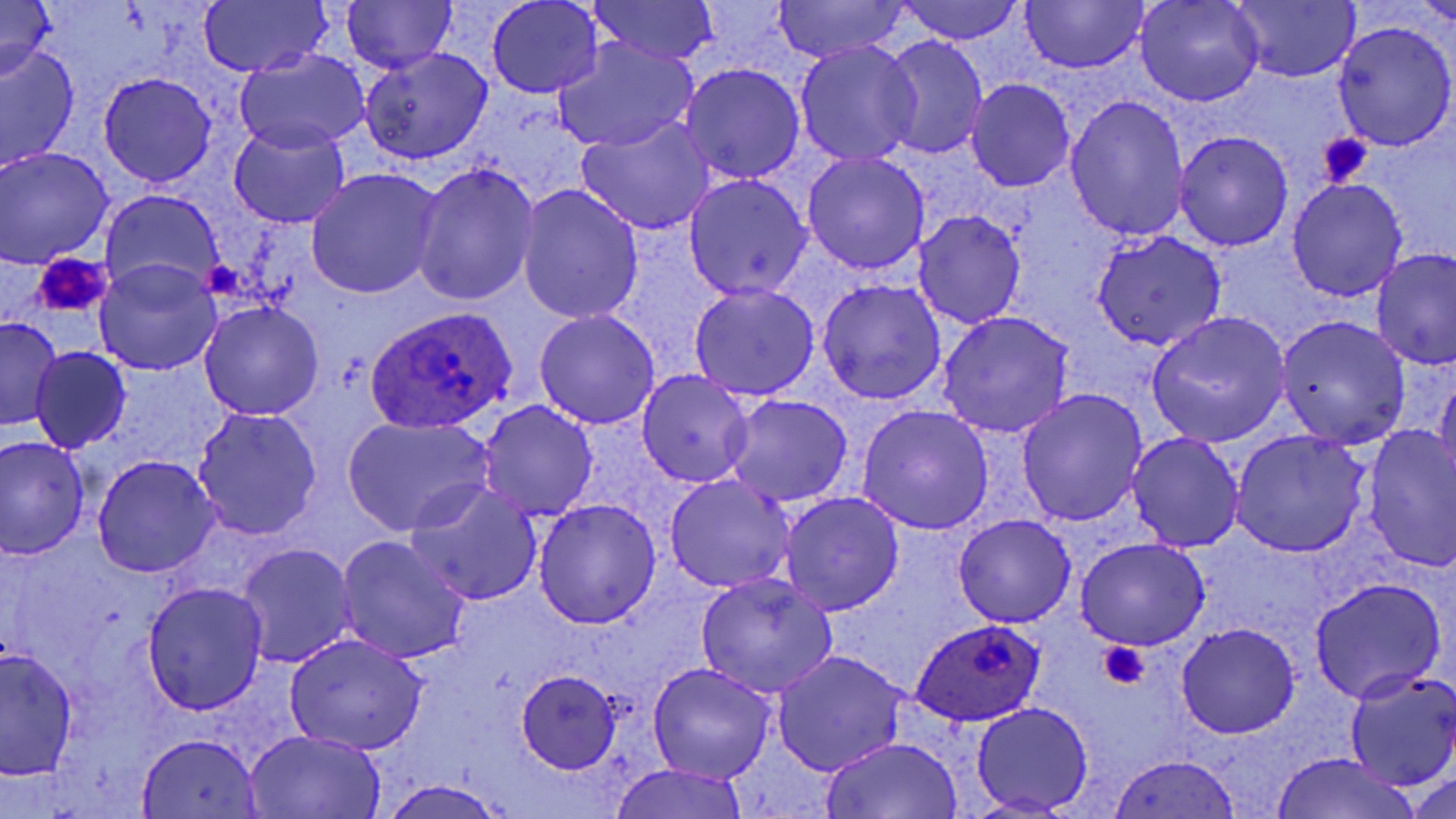

Summary:
  - Coordinate format: approximate bounding boxes as (x1, y1, x2, y2) in pixels
  - Plasmodium ovale-infected red blood cell locations: (367, 311, 518, 432), (911, 619, 1046, 727)
  - Uninfected red blood cell locations: (586, 0, 719, 69), (893, 0, 1025, 44), (1020, 0, 1147, 73), (1136, 0, 1264, 108), (1229, 0, 1359, 84), (0, 1, 57, 82), (342, 1, 456, 74), (486, 1, 603, 97), (196, 2, 330, 77), (772, 2, 910, 62), (1333, 21, 1456, 152), (879, 35, 990, 160), (553, 37, 702, 152), (794, 40, 922, 166), (1, 44, 78, 169), (360, 47, 491, 165), (235, 50, 371, 152), (680, 63, 805, 185), (96, 72, 217, 186), (966, 78, 1075, 192), (1065, 92, 1190, 242), (574, 117, 715, 236), (229, 121, 351, 228), (1173, 130, 1295, 252), (0, 146, 115, 267), (801, 153, 930, 275), (410, 164, 540, 305), (305, 168, 445, 299), (685, 173, 814, 300), (1286, 179, 1408, 301), (517, 184, 644, 325), (101, 187, 224, 299), (914, 210, 1025, 329), (1091, 232, 1226, 351), (1371, 249, 1456, 369), (95, 260, 219, 375), (816, 280, 946, 404), (689, 283, 820, 401), (199, 302, 323, 421), (532, 309, 661, 430), (938, 311, 1074, 438), (1146, 312, 1290, 448), (0, 316, 62, 430), (1276, 316, 1410, 450), (29, 347, 131, 453), (636, 371, 754, 489), (1436, 371, 1456, 485), (1016, 388, 1149, 525), (724, 394, 853, 506), (477, 400, 598, 520), (856, 404, 994, 535), (193, 407, 322, 540), (341, 416, 492, 537), (1362, 426, 1456, 571), (1230, 429, 1371, 557), (1126, 431, 1246, 554), (0, 435, 91, 558), (91, 456, 219, 577), (664, 473, 796, 593), (407, 482, 542, 607), (780, 491, 904, 616), (534, 498, 661, 628), (953, 512, 1076, 628), (336, 536, 469, 663), (1074, 538, 1210, 651), (236, 543, 357, 668), (696, 574, 839, 699), (1309, 579, 1444, 702), (142, 582, 267, 713), (1177, 622, 1299, 739), (284, 632, 428, 755), (1, 646, 77, 780), (772, 650, 910, 776), (648, 662, 776, 783), (1344, 667, 1456, 789), (516, 670, 620, 773), (971, 703, 1094, 814), (244, 730, 384, 818), (137, 731, 262, 817), (819, 736, 963, 817), (1268, 752, 1428, 819), (1106, 753, 1243, 818), (608, 762, 751, 819), (1410, 772, 1455, 817), (377, 777, 509, 819)
  - Platelet locations: (1318, 134, 1374, 185), (33, 253, 113, 318), (1098, 641, 1148, 688)
  - Slide-level diagnosis: Plasmodium ovale
  - Image size: 1456×819 pixels
  - Modality: light microscopy
  - Magnification: 1000x
  - Field of view: one of a larger specimen
  - Preparation: thin blood film
  - Stain: May-Grünwald-Giemsa